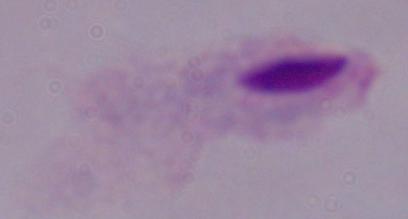

Summary:
  - Modality: micrograph
  - Identification: trichomonad
  - Magnification: 1000x